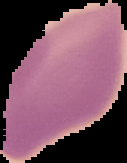
From a thin blood smear. Result: no malaria parasites detected. Segmented cell region on a black background. Image is 127×163 pixels.